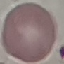

result = negative for malaria parasites
capture = smartphone through the microscope eyepiece
stain = Giemsa
image type = cell patch, automatically extracted from a larger field of view and resized to 64 × 64 pixels
preparation = thin blood film